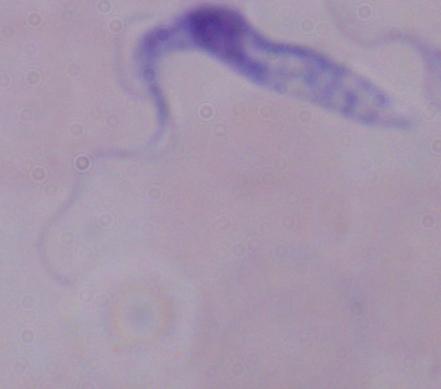 A trypanosome is seen. Captured at 1000x magnification. Photomicrograph.